Give the position of every malaria parasite.
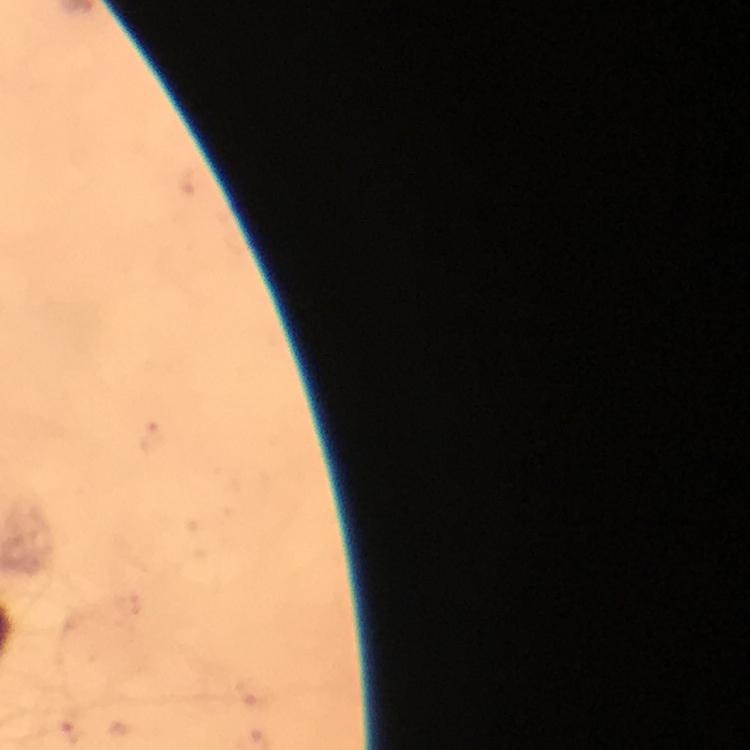

Approximate object centers, in pixels from the top-left corner.
Malaria parasites: (x=256, y=693), (x=71, y=731).

Summary:
  - Magnification: 100x
  - Stain: Giemsa
  - Cropped from: a single field of view
  - Image size: 750×750 pixels
  - Capture: smartphone mounted on the microscope
  - Context: from a diagnostic examination for malaria
  - Immersion oil: used
  - Preparation: thick blood smear